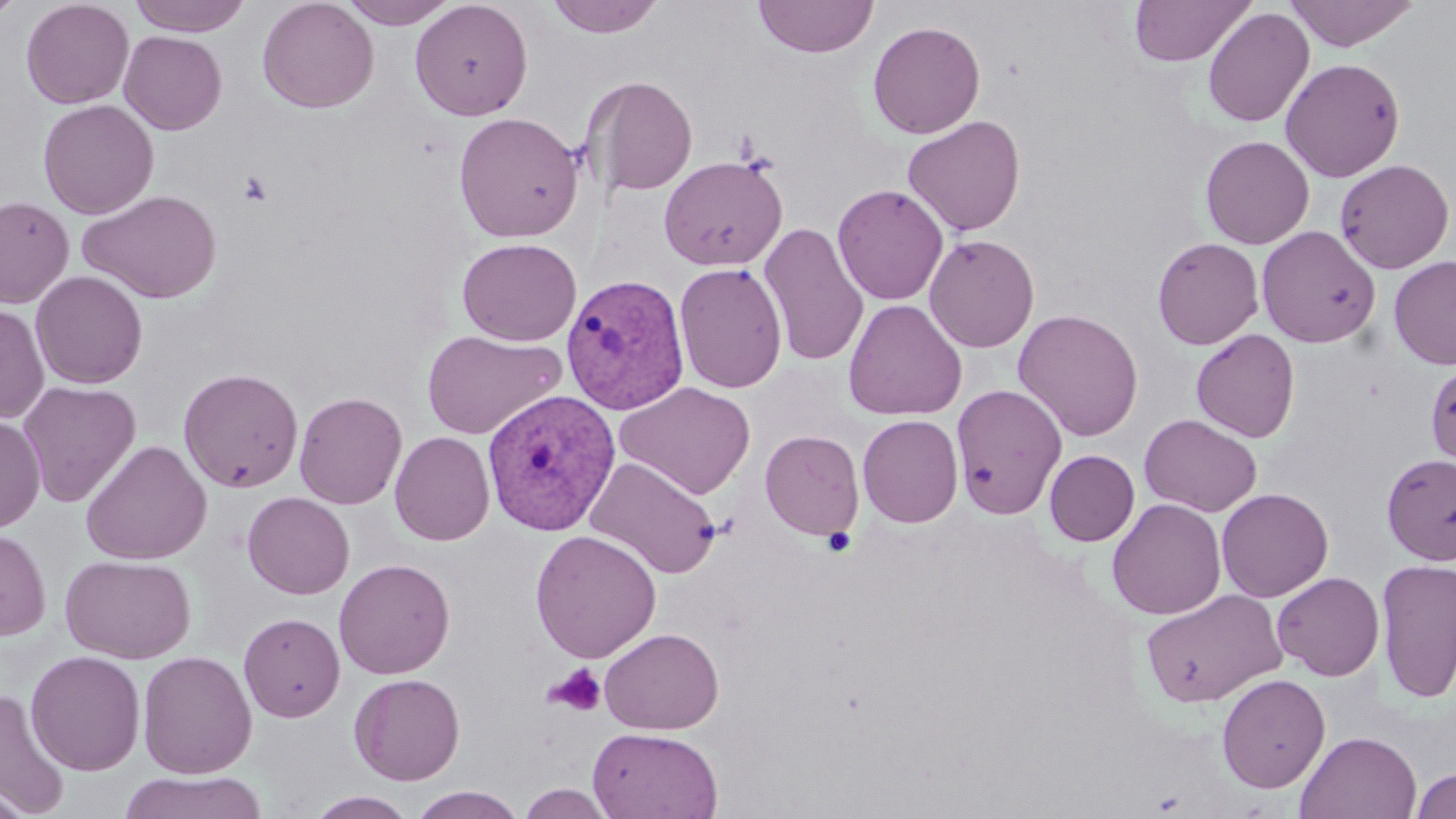

{
  "slide_level_diagnosis": "Plasmodium vivax",
  "image_size": "1456×819 pixels",
  "uninfected_red_blood_cell_locations": "approximate bounding boxes as [x1, y1, x2, y2] in pixels: [0, 0, 26, 24], [20, 0, 134, 109], [127, 0, 254, 36], [257, 0, 379, 114], [339, 0, 460, 28], [410, 0, 533, 121], [544, 0, 666, 38], [753, 0, 879, 59], [1284, 0, 1420, 51], [1128, 1, 1256, 66], [1202, 7, 1314, 128], [867, 20, 986, 139], [118, 30, 227, 135], [1280, 57, 1405, 181], [583, 74, 698, 196], [37, 99, 159, 219], [453, 111, 585, 243], [902, 115, 1026, 237], [1200, 135, 1315, 248], [659, 155, 788, 271], [1334, 158, 1454, 273], [832, 183, 949, 305], [79, 189, 222, 303], [0, 196, 74, 308], [758, 223, 870, 367], [1256, 225, 1381, 347], [923, 234, 1040, 352], [1152, 236, 1265, 350], [456, 237, 582, 346], [1389, 254, 1456, 370], [674, 262, 788, 394], [30, 270, 148, 389], [843, 299, 967, 420], [0, 302, 50, 425], [1013, 308, 1144, 441], [421, 328, 568, 440], [1191, 328, 1300, 442], [1425, 361, 1456, 468], [178, 367, 303, 493], [17, 381, 141, 507], [615, 381, 756, 499], [950, 383, 1068, 519], [294, 391, 407, 509], [0, 414, 44, 533], [857, 414, 963, 528], [1139, 414, 1262, 517], [389, 430, 495, 545], [760, 430, 865, 540], [80, 440, 212, 564], [1044, 449, 1139, 546], [1381, 452, 1456, 565], [586, 456, 720, 579], [1216, 487, 1334, 602], [242, 491, 355, 599], [1106, 498, 1227, 620], [0, 528, 51, 641], [530, 529, 663, 663], [60, 554, 196, 664], [333, 558, 455, 679], [1375, 558, 1456, 703], [1271, 571, 1385, 681], [1140, 588, 1287, 707], [238, 612, 346, 722], [599, 627, 724, 734], [25, 650, 146, 775], [137, 650, 258, 779], [349, 673, 465, 785], [1216, 673, 1330, 793], [0, 688, 72, 817], [588, 727, 723, 818], [1295, 730, 1422, 818], [1411, 767, 1456, 819], [119, 770, 269, 819], [0, 780, 33, 819], [518, 784, 616, 818], [407, 786, 527, 819], [305, 791, 418, 818]",
  "field_of_view": "single",
  "stain": "May-Grünwald-Giemsa",
  "preparation": "thin blood smear",
  "plasmodium_vivax_infected_red_blood_cell_locations": "approximate bounding boxes as [x1, y1, x2, y2] in pixels: [560, 273, 690, 415], [481, 389, 621, 535]",
  "platelet_locations": "approximate bounding boxes as [x1, y1, x2, y2] in pixels: [238, 170, 274, 206], [821, 527, 857, 557], [544, 663, 607, 718]",
  "modality": "light microscopy",
  "magnification": "1000x"
}